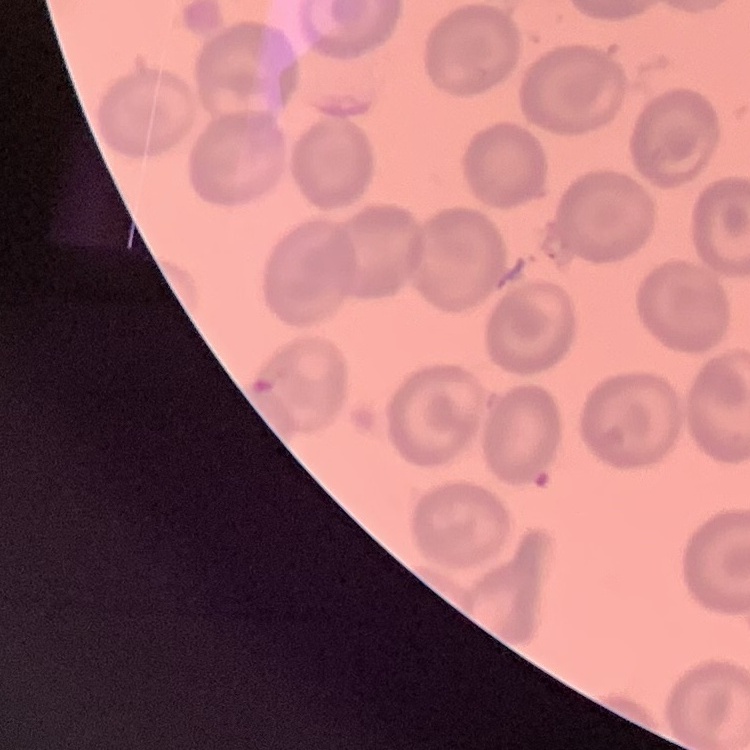
The red blood cells show no rouleaux formation. One tile cut from a larger photomicrograph. Thin blood smear. Field's or Giemsa stain.